Give the extent of all Plasmodium falciparum-infected red blood cells.
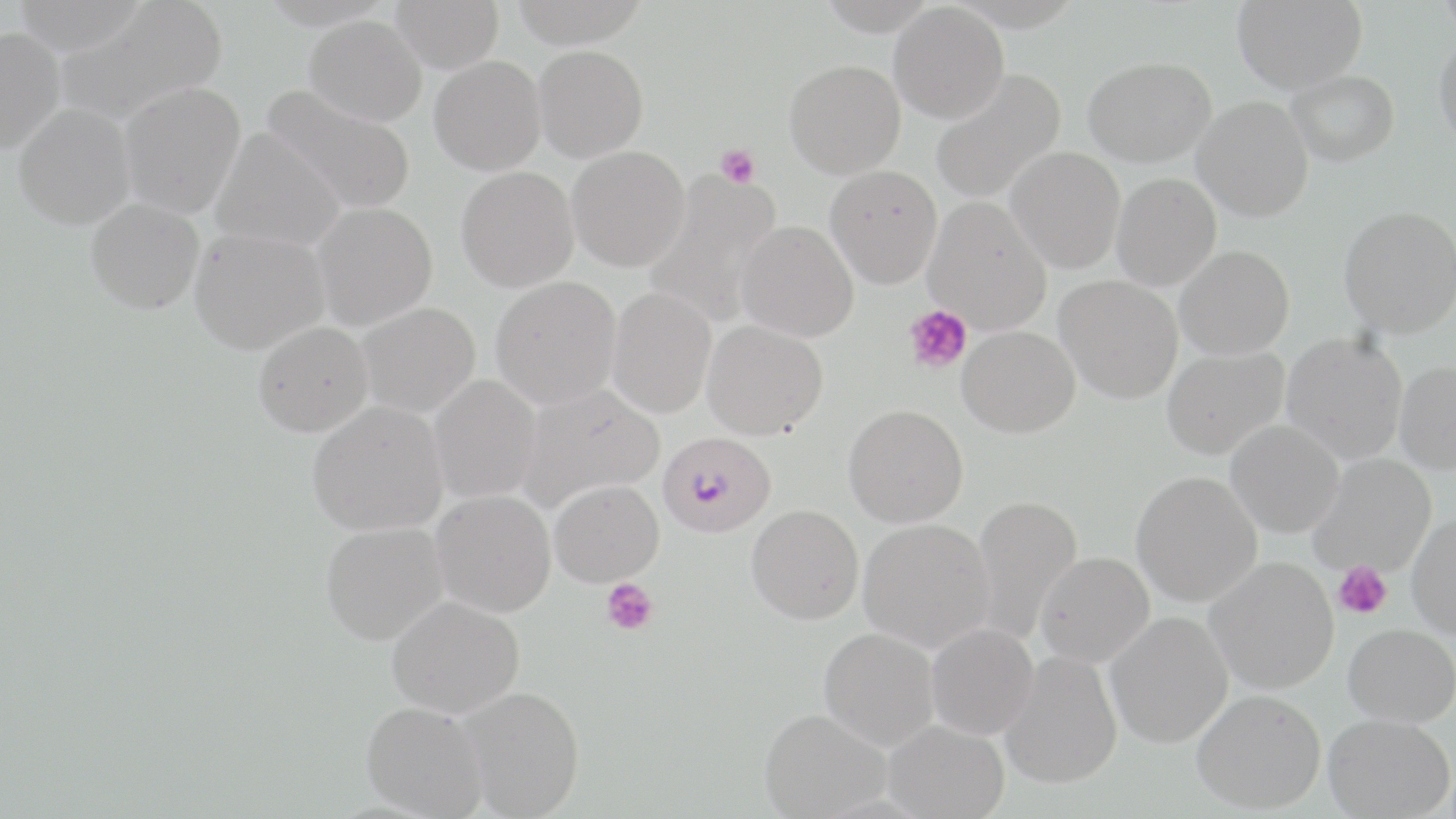

Approximate bounding boxes as [x1, y1, x2, y2] in pixels.
Plasmodium falciparum-infected red blood cells: [658, 430, 776, 538].

{
  "slide_level_diagnosis": "Plasmodium falciparum",
  "magnification": "1000x",
  "modality": "optical microscopy",
  "image_size": "1456×819 pixels",
  "uninfected_red_blood_cell_locations": "approximate bounding boxes as [x1, y1, x2, y2] in pixels: [10, 0, 151, 54], [391, 0, 504, 73], [509, 0, 651, 48], [1232, 0, 1368, 93], [1437, 0, 1456, 38], [55, 1, 228, 125], [889, 3, 1009, 123], [305, 15, 427, 126], [0, 26, 65, 154], [1434, 32, 1456, 150], [533, 45, 649, 162], [429, 56, 546, 175], [1084, 56, 1216, 167], [784, 60, 906, 178], [930, 69, 1066, 205], [1286, 70, 1399, 166], [119, 83, 246, 218], [261, 83, 417, 215], [1193, 97, 1313, 221], [13, 103, 136, 230], [211, 127, 346, 252], [567, 146, 690, 271], [1006, 147, 1125, 273], [825, 165, 942, 288], [456, 166, 579, 292], [644, 170, 784, 327], [1111, 173, 1221, 290], [924, 196, 1052, 335], [86, 198, 204, 314], [311, 202, 437, 329], [1338, 206, 1456, 337], [736, 220, 858, 342], [189, 226, 329, 354], [1174, 245, 1295, 359], [490, 276, 622, 410], [1055, 276, 1183, 403], [607, 287, 716, 418], [357, 302, 480, 418], [702, 319, 828, 439], [253, 322, 373, 437], [957, 325, 1080, 437], [1281, 331, 1408, 464], [1162, 347, 1288, 459], [1395, 360, 1456, 473], [427, 375, 542, 505], [517, 384, 664, 512], [307, 401, 448, 536], [843, 404, 968, 528], [1225, 420, 1344, 537], [1309, 454, 1436, 577], [1131, 470, 1262, 607], [550, 479, 664, 587], [431, 490, 556, 617], [971, 494, 1083, 644], [746, 504, 864, 624], [1407, 512, 1456, 639], [858, 518, 995, 652], [320, 522, 448, 645], [1035, 552, 1154, 667], [1205, 557, 1339, 694], [387, 596, 524, 718], [1105, 612, 1233, 748], [926, 622, 1038, 740], [1343, 623, 1456, 727], [819, 627, 939, 749], [1000, 650, 1122, 789], [459, 686, 584, 817], [1192, 689, 1326, 813], [361, 701, 489, 818], [759, 708, 890, 817], [1324, 714, 1454, 819], [883, 719, 1009, 818]",
  "platelet_locations": "approximate bounding boxes as [x1, y1, x2, y2] in pixels: [716, 143, 760, 188], [904, 305, 972, 374], [1334, 561, 1392, 619], [600, 578, 658, 636]",
  "field_of_view": "one of a larger specimen",
  "stain": "May-Grünwald-Giemsa",
  "preparation": "thin blood smear"
}